Point out each Plasmodium parasite.
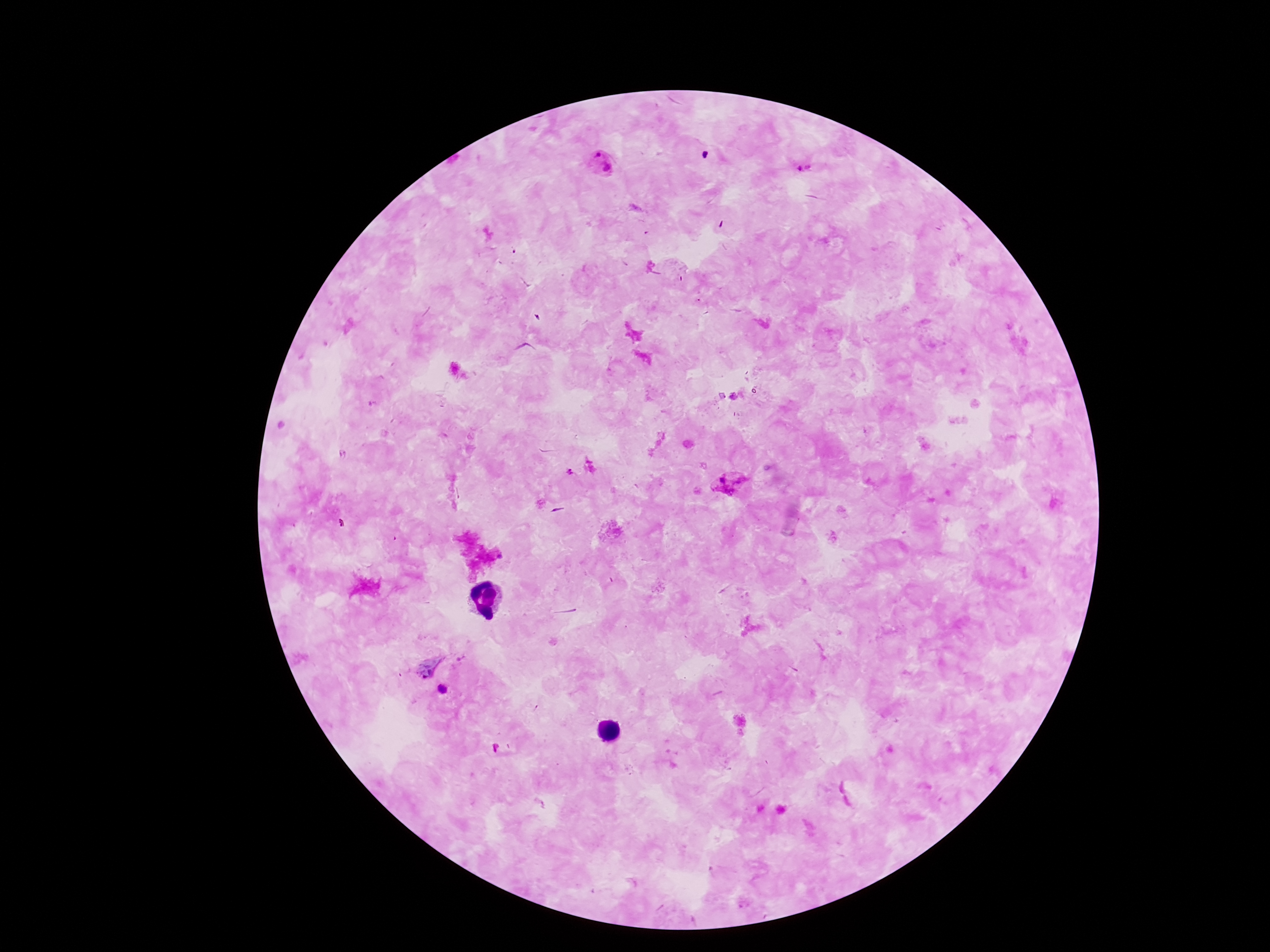
Approximate centers as {x, y} in pixels.
Plasmodium parasites: {603, 164}, {804, 167}, {570, 471}, {729, 483}, {442, 689}.

Summary:
  - Patient malaria status: positive
  - Capture: smartphone camera through the microscope eyepiece
  - Preparation: thick blood film
  - Magnification: 100x
  - Stain: Giemsa
  - Field of view: single
  - Image size: 1270×952 pixels